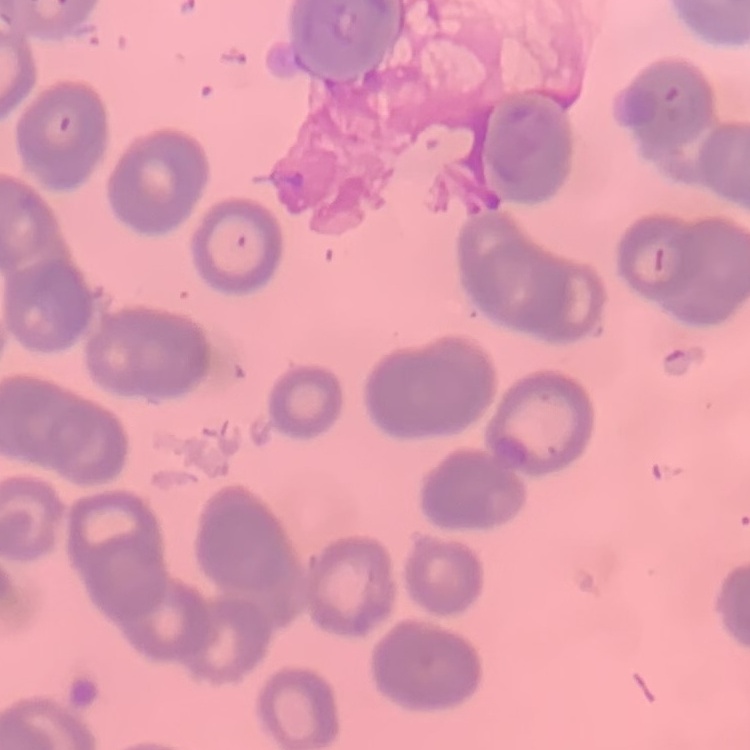 The red blood cells show rouleaux formation. Square crop of a larger photomicrograph. Thin blood film. Stained with either Field's or Giemsa.